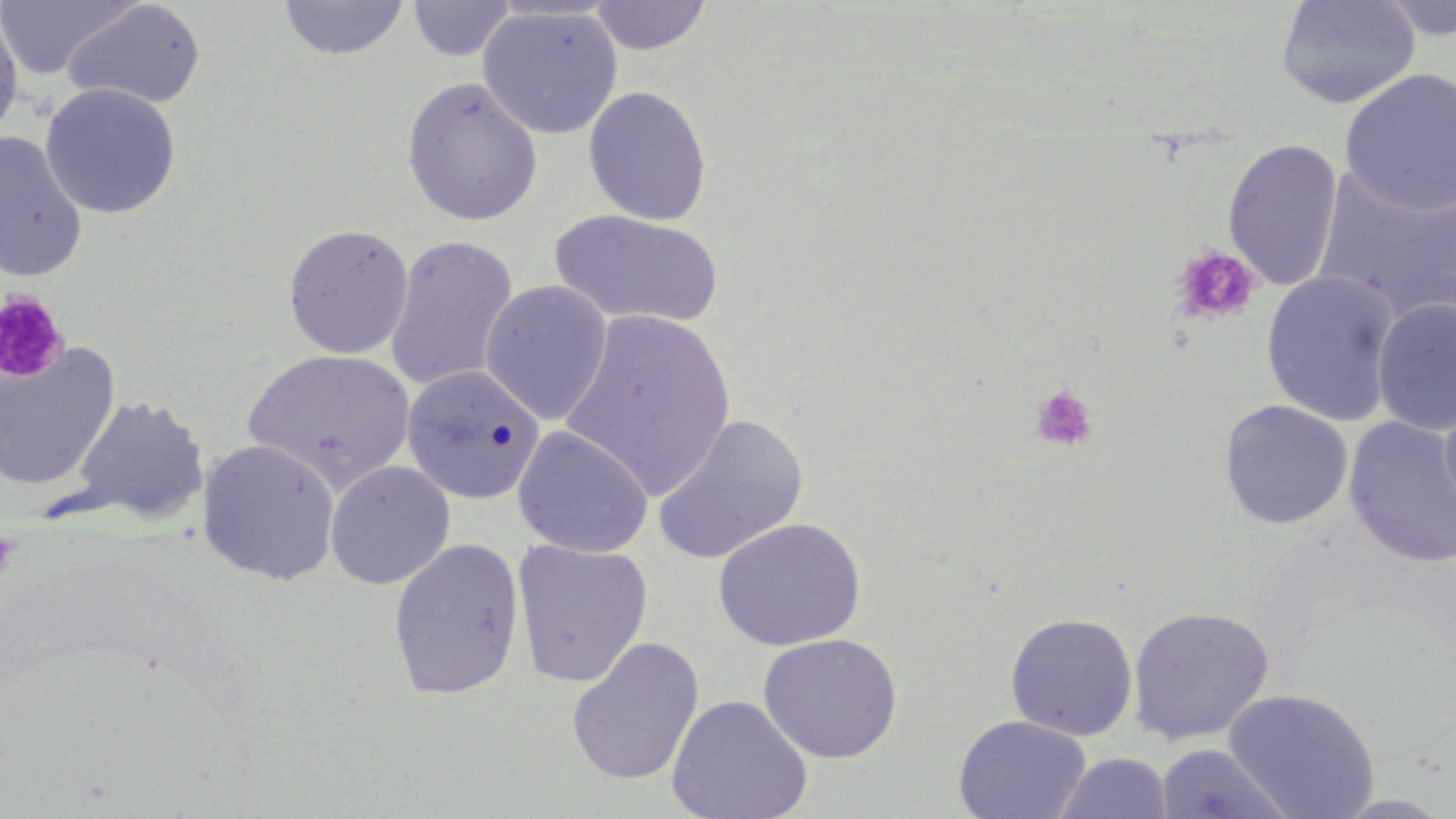
slide-level diagnosis = negative for blood parasites
image size = 1456×819 pixels
field of view = single
magnification = 1000x
modality = light microscopy
preparation = thin blood smear
stain = May-Grünwald-Giemsa
platelet locations = approximate bounding boxes as (x1, y1, x2, y2) in pixels: (1170, 245, 1261, 328), (0, 291, 69, 383), (1029, 383, 1099, 453)
uninfected red blood cell locations = approximate bounding boxes as (x1, y1, x2, y2) in pixels: (278, 0, 410, 61), (588, 0, 713, 55), (1275, 0, 1422, 110), (1376, 0, 1456, 41), (0, 1, 141, 80), (61, 1, 207, 111), (407, 1, 516, 60), (477, 5, 623, 140), (0, 8, 25, 143), (1339, 69, 1455, 216), (400, 76, 543, 226), (40, 82, 181, 219), (583, 85, 713, 227), (0, 131, 89, 282), (1223, 138, 1343, 292), (1314, 165, 1456, 318), (550, 209, 724, 330), (282, 222, 415, 359), (385, 234, 518, 392), (1261, 270, 1401, 426), (479, 279, 614, 424), (1372, 298, 1456, 435), (560, 309, 737, 497), (0, 344, 120, 490), (244, 348, 416, 489), (401, 364, 546, 505), (1439, 384, 1456, 532), (67, 395, 209, 526), (1219, 399, 1353, 530), (651, 413, 809, 565), (1344, 417, 1456, 569), (513, 425, 654, 558), (197, 439, 341, 585), (324, 460, 456, 590), (712, 517, 866, 652), (387, 536, 525, 699), (512, 539, 654, 687), (1126, 605, 1275, 746), (1004, 612, 1139, 741), (758, 633, 903, 763), (566, 636, 705, 786), (1223, 688, 1381, 819), (667, 694, 813, 819), (953, 714, 1091, 819), (1156, 743, 1294, 819), (1053, 752, 1173, 819)